Describe the morphology of the erythrocytes.
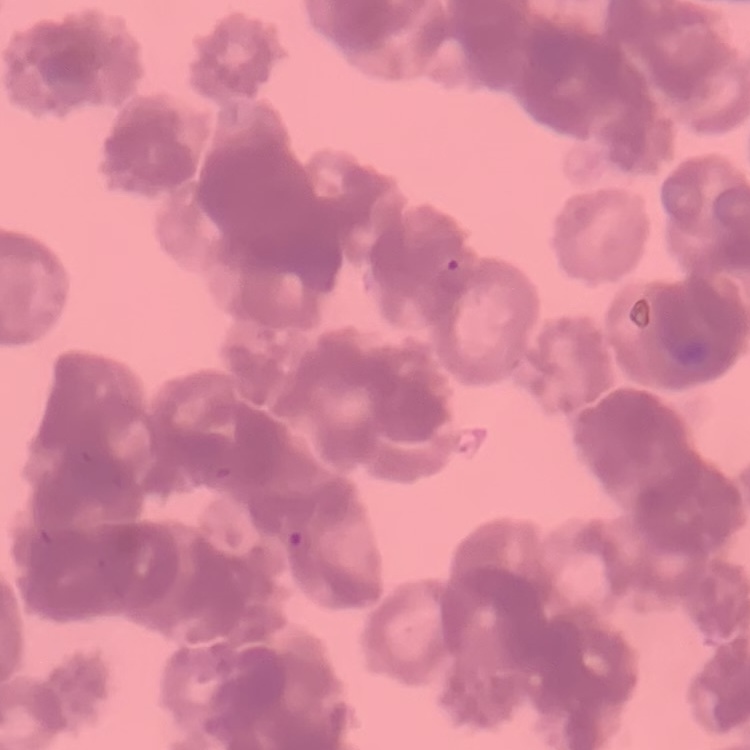
Rouleaux formation.

Summary:
  - Stain: Field's or Giemsa
  - Preparation: thin peripheral smear
  - Image type: one tile cut from a larger photomicrograph